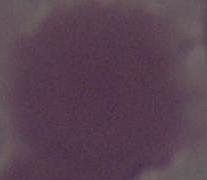 A red blood cell is shown. Captured at 1000x magnification. Photomicrograph.